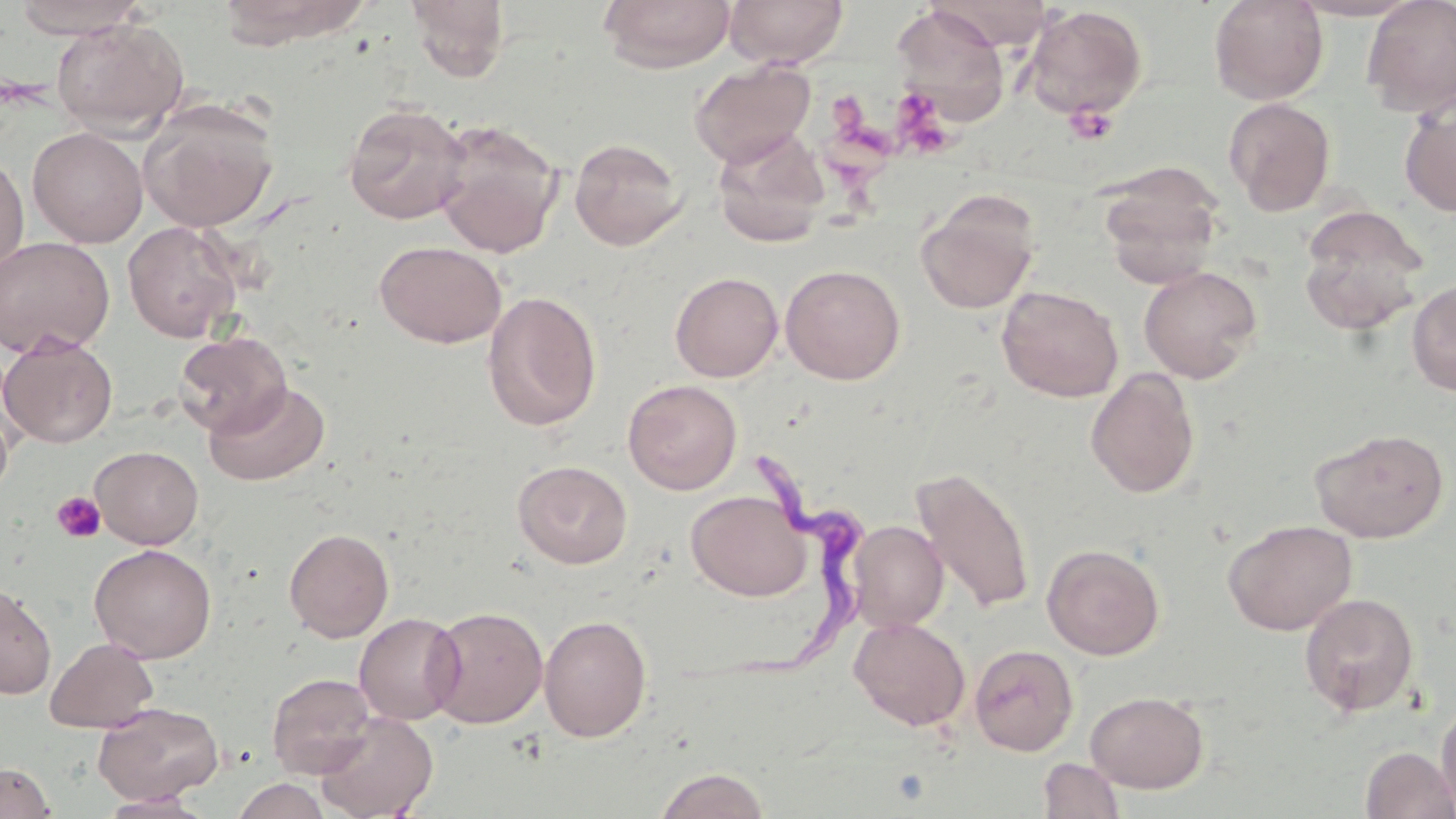
Summary:
  - Coordinate format: approximate bounding boxes as [x1, y1, x2, y2] in pixels
  - Trypanosoma brucei locations: [725, 450, 875, 688]
  - Platelet locations: [896, 96, 955, 156], [1065, 104, 1118, 145], [51, 492, 106, 543]
  - Uninfected red blood cell locations: [11, 0, 151, 39], [217, 0, 368, 47], [598, 0, 735, 73], [724, 0, 850, 69], [1208, 0, 1329, 105], [1286, 0, 1427, 21], [1361, 0, 1456, 117], [406, 1, 510, 82], [892, 4, 1009, 123], [1022, 5, 1148, 120], [51, 17, 189, 137], [689, 60, 816, 169], [1223, 97, 1336, 215], [138, 99, 278, 232], [1399, 99, 1456, 217], [343, 101, 471, 224], [433, 120, 564, 258], [27, 127, 148, 248], [712, 129, 830, 247], [568, 137, 688, 250], [0, 153, 29, 277], [1099, 170, 1224, 287], [918, 193, 1039, 313], [1297, 206, 1429, 335], [122, 220, 244, 342], [0, 237, 115, 358], [375, 241, 507, 348], [780, 263, 906, 384], [1139, 266, 1263, 383], [669, 271, 783, 382], [1406, 279, 1456, 397], [996, 285, 1124, 402], [481, 290, 602, 432], [173, 331, 292, 437], [1, 335, 118, 448], [1085, 369, 1201, 498], [205, 379, 331, 486], [623, 379, 742, 495], [0, 403, 14, 501], [1310, 427, 1451, 542], [90, 445, 204, 549], [513, 460, 632, 569], [913, 465, 1035, 614], [686, 489, 812, 601], [1222, 519, 1358, 635], [848, 521, 949, 632], [284, 528, 394, 642], [1042, 543, 1165, 660], [89, 544, 216, 663], [0, 584, 57, 699], [1298, 592, 1420, 718], [425, 606, 548, 728], [354, 612, 465, 725], [539, 614, 652, 742], [848, 616, 971, 731], [45, 637, 159, 732], [969, 643, 1078, 756], [266, 672, 378, 779], [1085, 691, 1208, 793], [1436, 698, 1456, 817], [92, 702, 224, 805], [314, 711, 438, 819], [1359, 745, 1456, 819], [1038, 757, 1124, 818], [0, 761, 55, 818], [652, 767, 772, 818], [232, 777, 332, 819], [98, 791, 213, 817]
  - Slide-level diagnosis: Trypanosoma brucei
  - Preparation: thin blood smear
  - Image size: 1456×819 pixels
  - Modality: light microscopy
  - Magnification: 1000x
  - Field of view: single
  - Stain: May-Grünwald-Giemsa